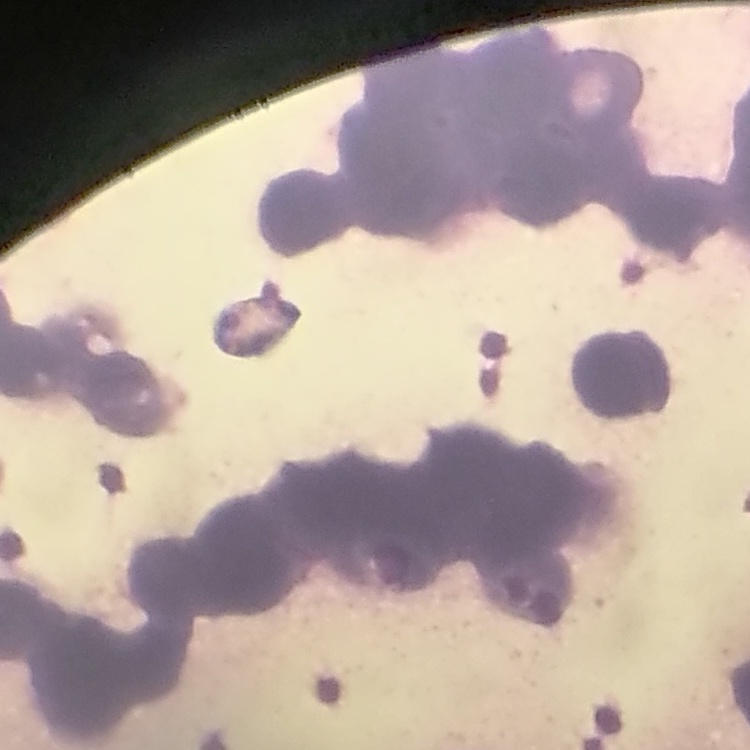
Summary:
  - Red blood cell morphology: rouleaux formation
  - Stain: Field's or Giemsa
  - Preparation: thin blood smear
  - Image type: one tile cut from a larger photomicrograph